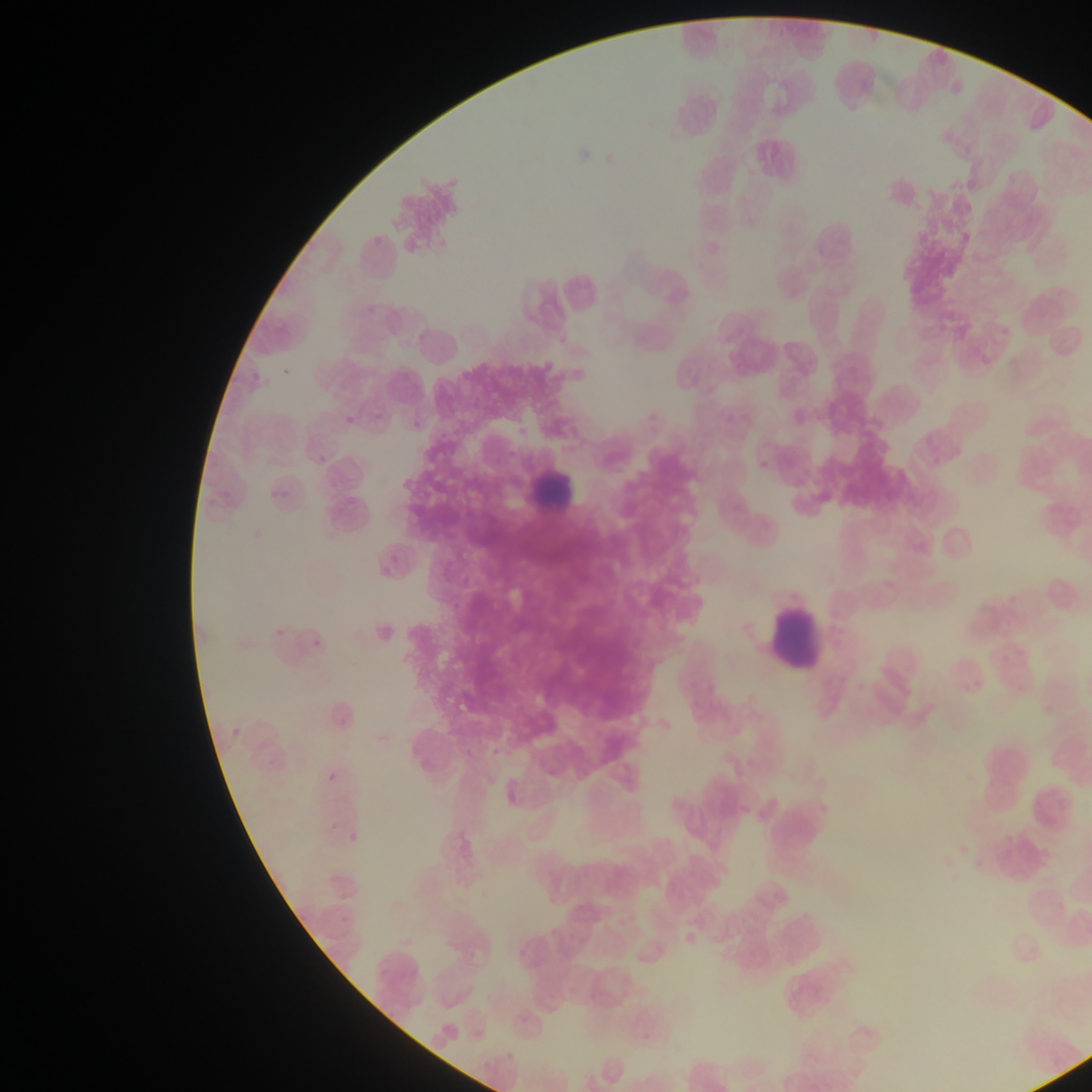
Approximate bounding boxes as left top right bottom in pixels. Malaria parasite locations: 371 409 388 427. Leukocyte locations: 518 450 577 507; 761 595 829 678. Image is 1092×1092 pixels. Single field of view. Sample from Ghana. Photographed through a microscope with a mobile-phone camera. Thin blood film.